Give the position of every malaria parasite.
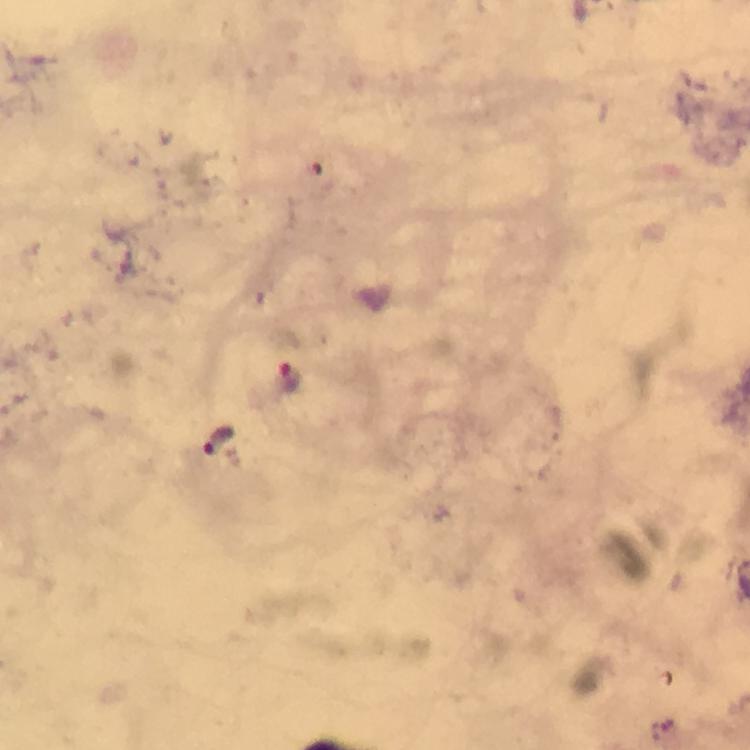

Approximate centers as {x, y} in pixels.
Malaria parasites: {289, 378}, {221, 439}.

Summary:
  - Context: from a malaria diagnostic workup
  - Cropped from: a single field of view
  - Capture: smartphone photograph through a microscope
  - Image size: 750×750 pixels
  - Magnification: 100x
  - Immersion oil: used
  - Preparation: thick blood film
  - Stain: Giemsa